Outline each P. falciparum parasite and classify it by life-cycle stage.
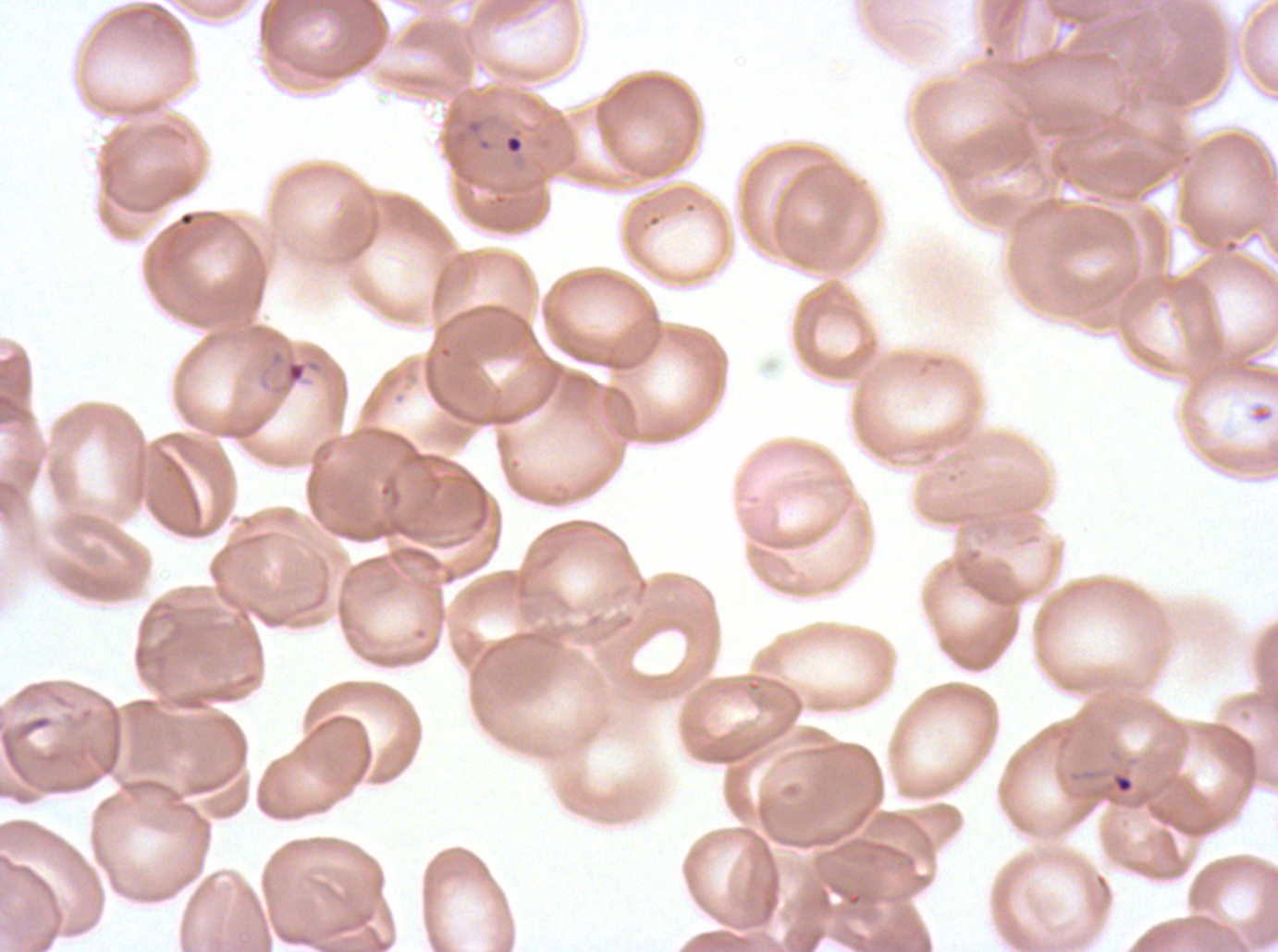
Approximate bounding rectangles given as corner coordinates in pixels from the top-left.
Rings: (x1=503, y1=133, x2=524, y2=155), (x1=283, y1=358, x2=323, y2=388), (x1=1112, y1=773, x2=1135, y2=795).
No late-ring/early-trophozoite forms, mid trophozoites, late trophozoites, early schizonts, late schizonts, segmenters, or gametocytes observed.

stain = Giemsa
specimen = P. falciparum from a patient in The Gambia, cultured ex vivo for 24 to 48 hours
preparation = thin blood film
field of view = sub-image separated from a larger composite
image size = 1278×952 pixels